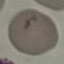
result = no malaria parasites detected
stain = Giemsa
preparation = thin blood smear
capture = smartphone camera at the microscope eyepiece
image type = cell patch, automatically extracted from a larger field of view and resized to 64 × 64 pixels